Locate every blood parasite and identify its species.
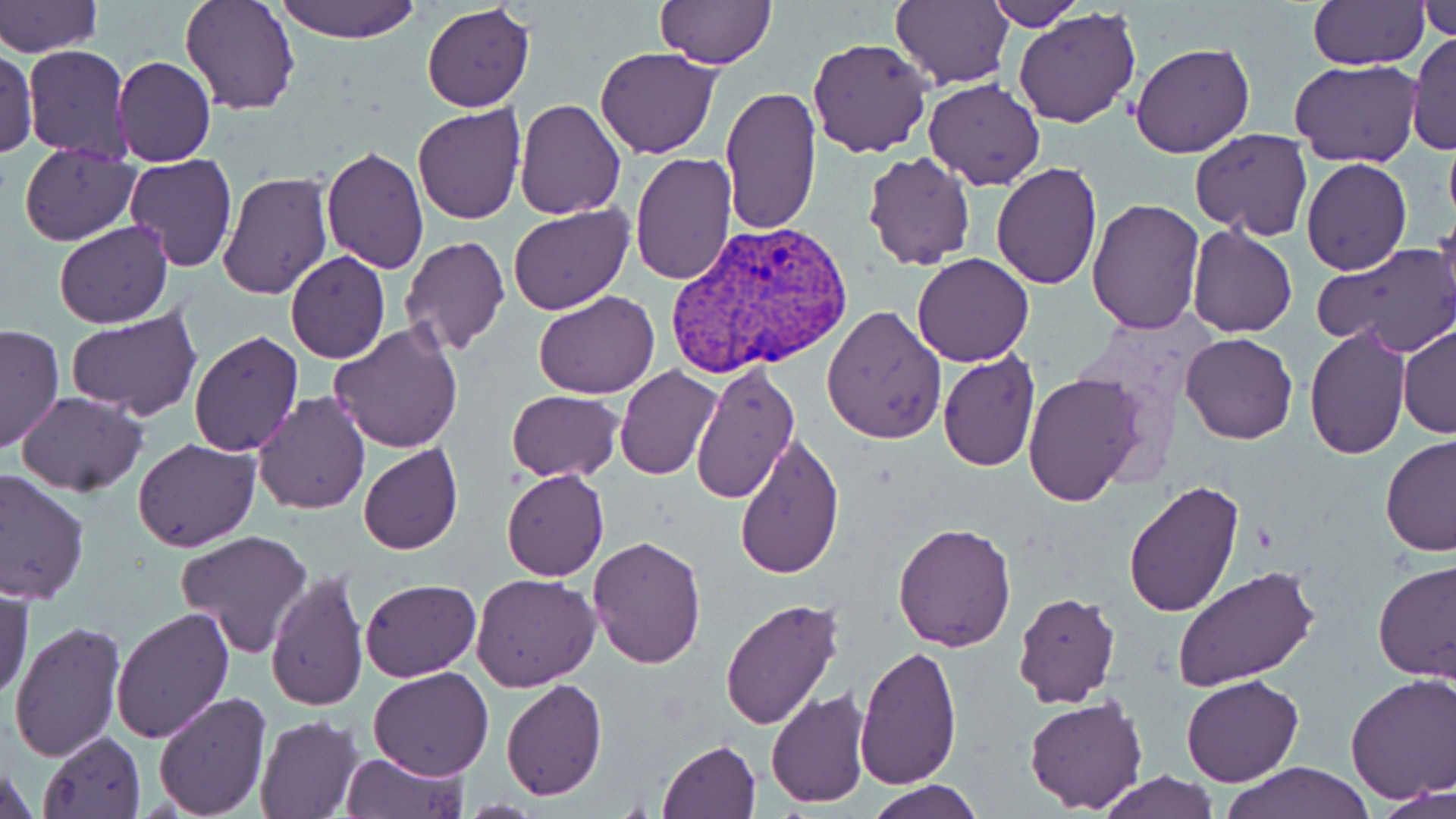
Approximate bounding boxes as (x1, y1, x2, y2) in pixels.
Plasmodium vivax-infected red blood cells: (665, 220, 858, 378).
No Plasmodium falciparum, Plasmodium ovale, Plasmodium malariae, Babesia divergens, or Trypanosoma brucei observed.

slide-level diagnosis = Plasmodium vivax
magnification = 1000x
modality = optical microscopy
uninfected red blood cell locations = approximate bounding boxes as (x1, y1, x2, y2) in pixels: (179, 0, 301, 115), (275, 0, 422, 44), (890, 0, 1012, 90), (982, 0, 1083, 30), (0, 1, 101, 56), (1307, 1, 1428, 69), (1418, 1, 1455, 42), (655, 2, 777, 68), (422, 3, 535, 112), (1015, 8, 1142, 129), (1406, 33, 1456, 158), (806, 36, 933, 158), (1131, 41, 1255, 159), (21, 46, 132, 161), (594, 47, 720, 159), (1, 49, 36, 159), (112, 56, 216, 167), (1291, 59, 1422, 166), (924, 78, 1045, 192), (721, 86, 821, 235), (514, 99, 626, 221), (413, 103, 525, 224), (1190, 127, 1313, 238), (936, 133, 1075, 281), (19, 143, 140, 245), (321, 146, 428, 275), (862, 151, 977, 270), (631, 152, 737, 285), (122, 154, 236, 272), (1302, 158, 1410, 275), (991, 161, 1103, 289), (216, 170, 335, 300), (1087, 198, 1205, 334), (508, 204, 632, 313), (1434, 213, 1456, 324), (54, 222, 174, 328), (1187, 224, 1297, 339), (400, 236, 510, 357), (1313, 242, 1456, 356), (284, 251, 390, 363), (912, 252, 1035, 367), (305, 269, 435, 418), (533, 289, 658, 399), (66, 305, 203, 421), (822, 305, 946, 446), (1, 322, 62, 454), (329, 322, 465, 452), (1398, 322, 1456, 439), (1303, 325, 1411, 462), (189, 332, 305, 458), (1180, 333, 1297, 443), (937, 349, 1041, 470), (689, 364, 799, 505), (615, 367, 721, 480), (1023, 372, 1148, 509), (506, 390, 626, 482), (15, 391, 148, 495), (251, 391, 373, 514), (733, 431, 845, 581), (1380, 434, 1456, 558), (132, 438, 259, 553), (359, 443, 463, 555), (0, 469, 91, 605), (501, 469, 610, 581), (1123, 479, 1244, 618), (893, 521, 1017, 651), (173, 530, 315, 660), (588, 535, 707, 668), (1373, 560, 1455, 682), (265, 567, 370, 712), (1172, 567, 1319, 691), (471, 573, 601, 692), (359, 577, 481, 682), (0, 580, 34, 706), (1013, 593, 1121, 709), (720, 599, 844, 730), (110, 607, 234, 744), (8, 621, 126, 763), (853, 644, 963, 790), (367, 668, 495, 781), (1346, 673, 1456, 805), (1181, 675, 1304, 788), (500, 679, 607, 800), (764, 688, 871, 808), (152, 689, 271, 816), (1023, 694, 1149, 814), (253, 716, 363, 817), (38, 731, 146, 818), (658, 739, 761, 819), (338, 750, 469, 818), (1222, 760, 1374, 818), (0, 761, 39, 819), (1096, 769, 1219, 819), (867, 780, 983, 819), (1377, 781, 1454, 819)
preparation = thin blood smear
image size = 1456×819 pixels
field of view = single
stain = May-Grünwald-Giemsa